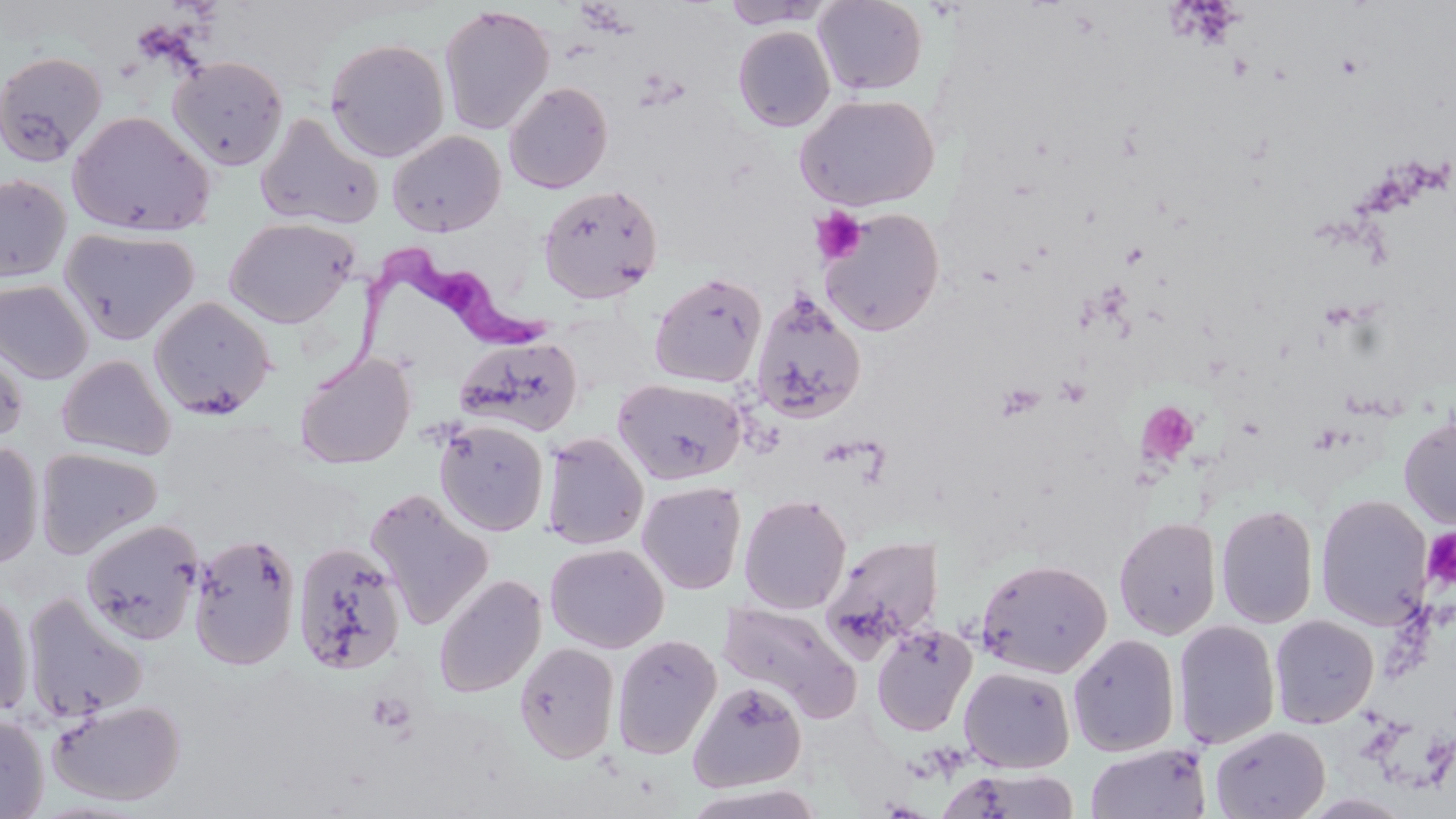

Summary:
  - Coordinate format: approximate bounding boxes as (x1, y1, x2, y2) in pixels
  - Trypanosoma brucei locations: (314, 243, 560, 393)
  - Platelet locations: (810, 208, 867, 264), (1120, 241, 1149, 270), (1055, 377, 1090, 409), (995, 381, 1045, 423), (1137, 400, 1200, 468), (1423, 527, 1456, 588), (365, 691, 416, 738)
  - Uninfected red blood cell locations: (812, 0, 929, 96), (720, 1, 834, 29), (438, 4, 555, 135), (732, 25, 836, 132), (324, 37, 450, 162), (0, 51, 107, 165), (167, 55, 289, 172), (503, 81, 613, 194), (795, 93, 941, 211), (67, 110, 216, 237), (255, 111, 384, 230), (387, 130, 506, 237), (0, 173, 73, 282), (537, 183, 664, 304), (819, 208, 945, 336), (222, 216, 360, 328), (59, 226, 199, 345), (649, 272, 767, 388), (0, 279, 94, 384), (749, 291, 867, 425), (148, 296, 277, 419), (454, 335, 585, 436), (0, 338, 30, 448), (295, 352, 416, 469), (56, 355, 176, 460), (614, 377, 746, 484), (1398, 412, 1456, 530), (434, 419, 549, 536), (540, 432, 649, 550), (0, 441, 44, 570), (34, 446, 162, 559), (636, 481, 746, 594), (364, 487, 495, 631), (739, 494, 852, 614), (1315, 494, 1434, 629), (1215, 503, 1319, 629), (1113, 516, 1222, 639), (80, 518, 205, 645), (188, 532, 302, 671), (822, 534, 945, 658), (292, 541, 408, 676), (544, 543, 669, 653), (976, 558, 1112, 678), (433, 574, 547, 698), (0, 587, 34, 721), (21, 592, 148, 723), (719, 600, 862, 723), (1269, 614, 1379, 728), (1172, 620, 1281, 749), (871, 623, 977, 737), (1067, 633, 1180, 757), (612, 634, 721, 759), (514, 641, 620, 764), (958, 666, 1075, 773), (688, 680, 807, 792), (48, 698, 186, 806), (0, 713, 49, 818), (1209, 724, 1330, 819), (1085, 743, 1211, 819), (938, 767, 1081, 819), (681, 784, 826, 819)
  - Slide-level diagnosis: Trypanosoma brucei
  - Preparation: thin blood smear
  - Field of view: single
  - Modality: light microscopy
  - Magnification: 1000x
  - Stain: May-Grünwald-Giemsa
  - Image size: 1456×819 pixels